Assess the morphology of the red blood cells.
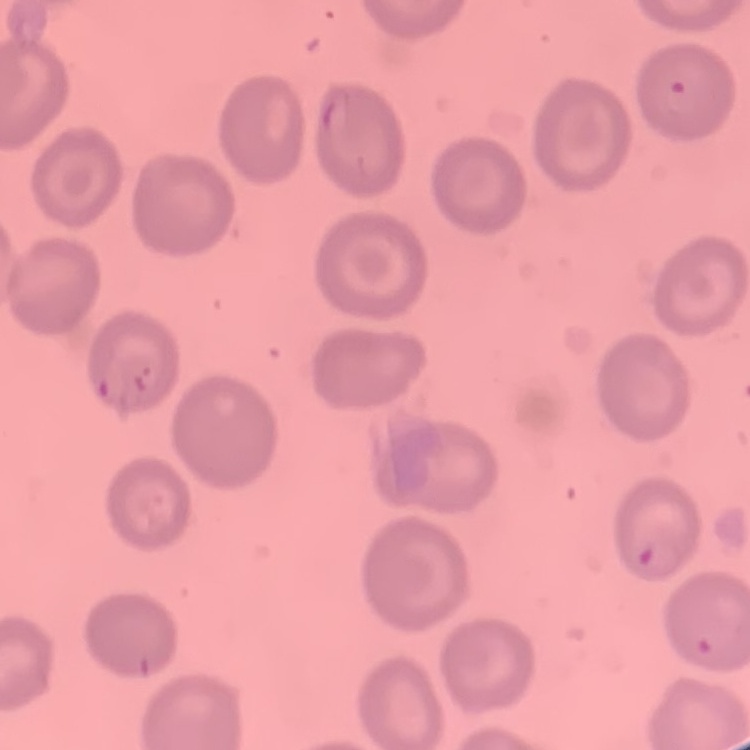
They show no rouleaux formation.

Thin blood smear. One tile cut from a larger photomicrograph. Stained with either Field's or Giemsa.